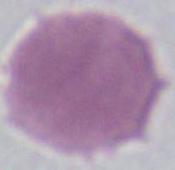 Photomicrograph. An erythrocyte is seen. Captured at 1000x magnification.